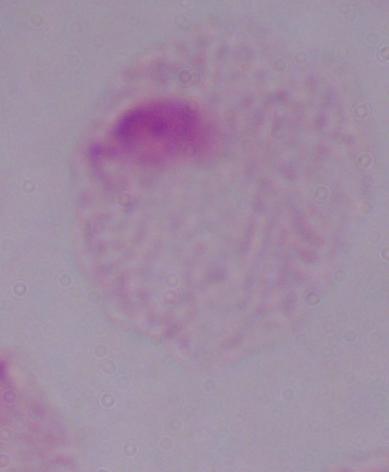

Summary:
  - Magnification: 1000x
  - Modality: micrograph
  - Identification: trichomonad